Classify this cell by malaria status.
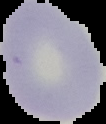
It is uninfected.

Image is 106×124 pixels. Cell region segmented out of the field of view; the surrounding area is masked to black. From a thin blood smear.